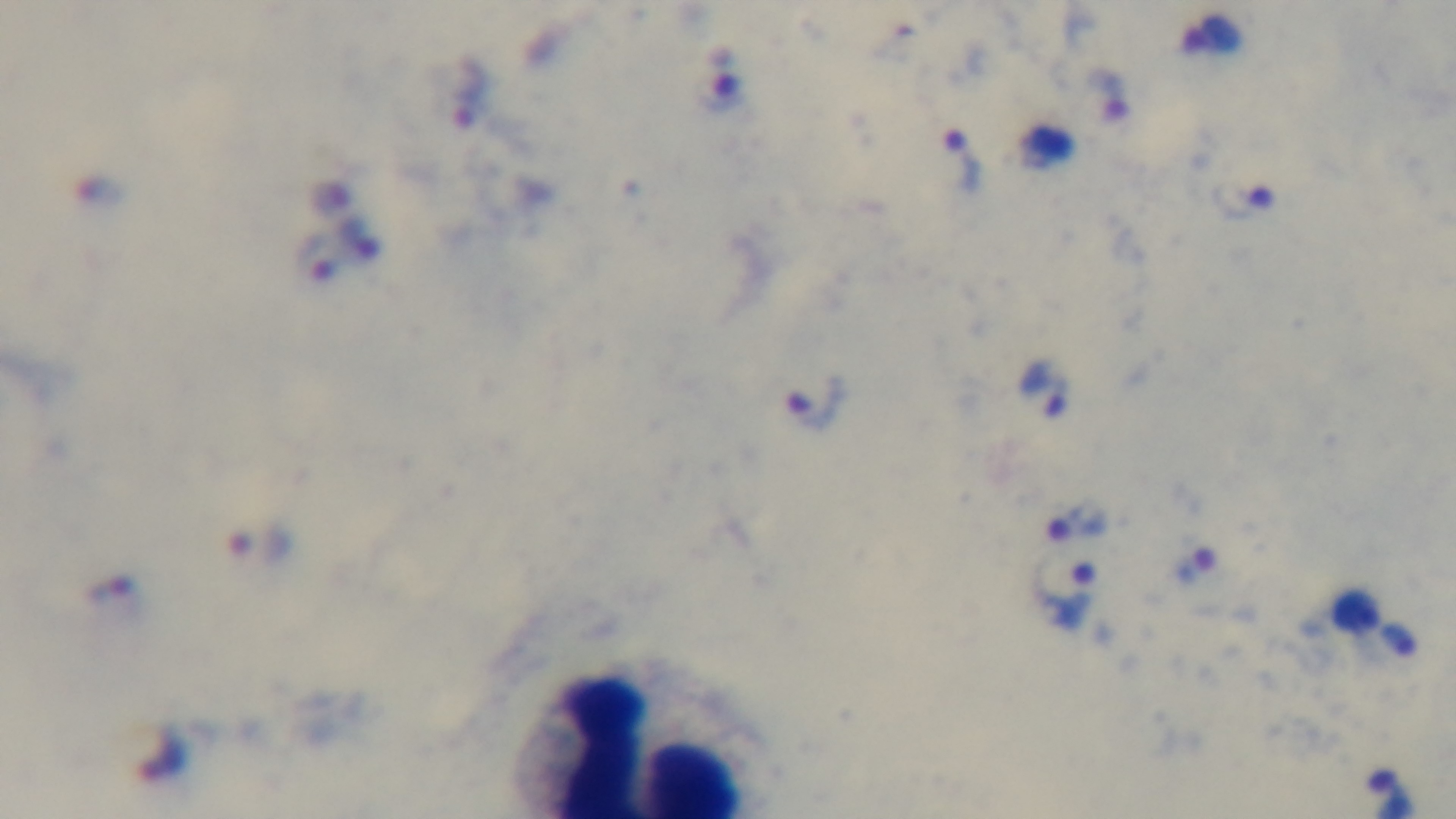
Summary:
  - Stain: Giemsa
  - Preparation: thick
  - Modality: light microscopy
  - Malaria status: infected
  - Field of view: one from the slide
  - Objective: 100x oil immersion
  - Capture: mounted 4K digital camera